Report the malaria status of this cell.
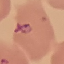
It is parasitized.

Summary:
  - Image type: automatically extracted cell patch, resized to 64 × 64 pixels
  - Capture: smartphone camera at the microscope eyepiece
  - Stain: Giemsa
  - Preparation: thin smear